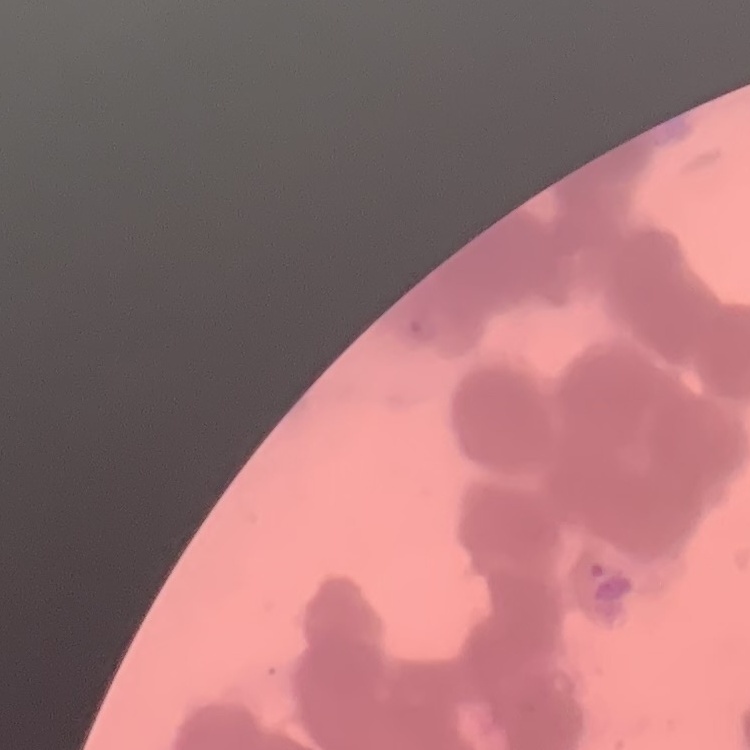

Summary:
  - Red blood cell morphology: rouleaux formation
  - Preparation: thin peripheral smear
  - Image type: one tile cut from a larger photomicrograph
  - Stain: Field's or Giemsa